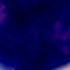
Photomicrograph. 1000x magnification. A white blood cell is seen.